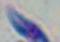
modality = photomicrograph
magnification = 1000x
identification = Toxoplasma gondii